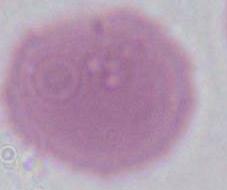

Summary:
  - Identification: erythrocyte
  - Modality: photomicrograph
  - Magnification: 1000x